Classify this cell by malaria status.
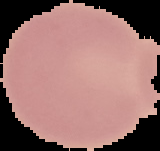
Uninfected.

image size = 160×151 pixels
preparation = thin blood smear
image type = segmented cell region on a black background